Look for Plasmodium parasites.
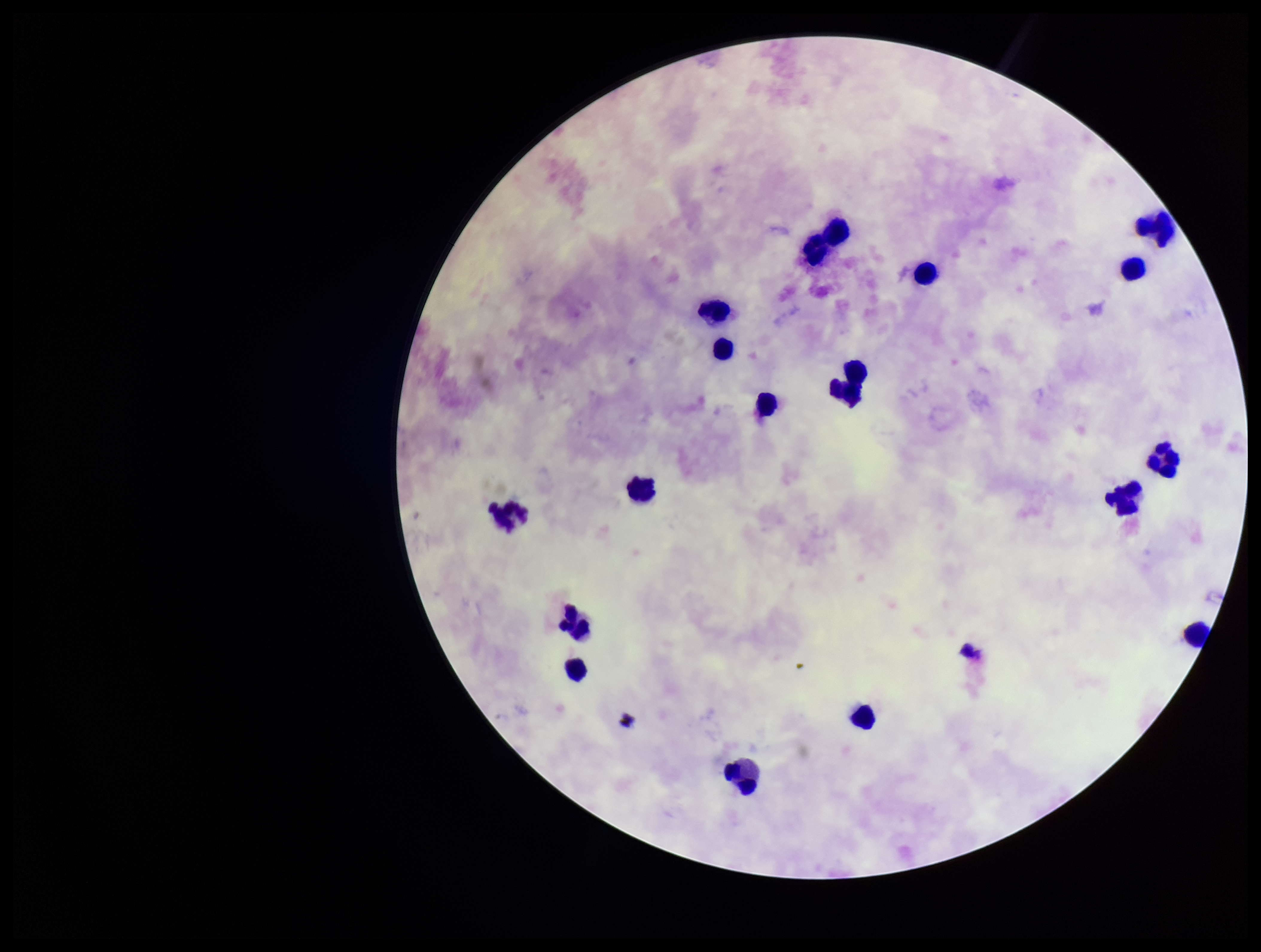
None detected.

Summary:
  - Capture: smartphone photograph through the microscope eyepiece
  - Preparation: thick blood smear
  - Parasite count: 0
  - Leukocyte count: 18
  - Image size: 1261×952 pixels
  - Patient malaria status: negative
  - Stain: Giemsa
  - Field of view: one from this slide